Outline each uninfected red blood cell.
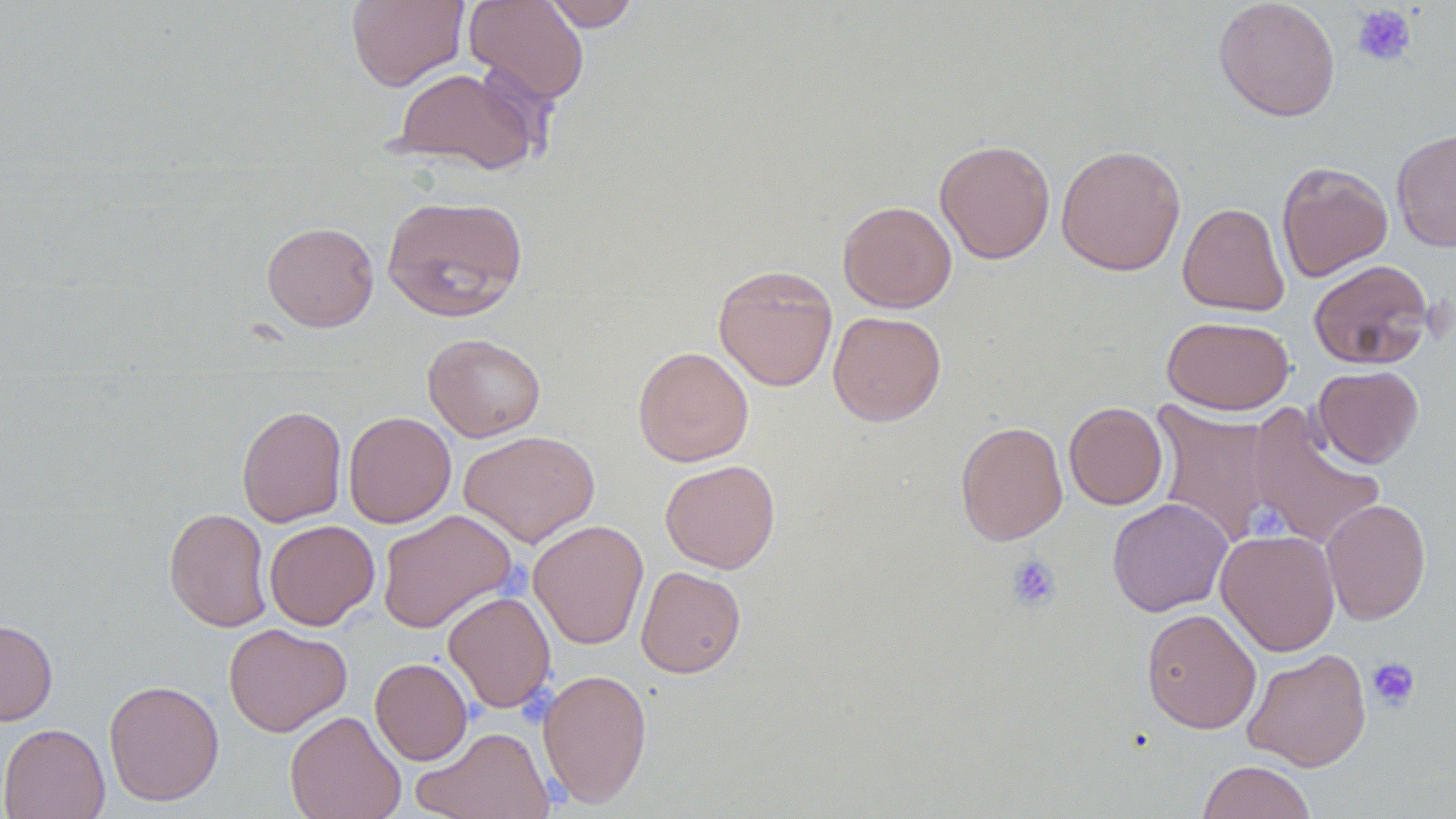
Approximate bounding boxes as named x1/y1/x2/y2 corners in pixels.
Uninfected red blood cells: (x1=346, y1=0, x2=469, y2=91), (x1=464, y1=0, x2=590, y2=105), (x1=540, y1=0, x2=641, y2=31), (x1=1213, y1=0, x2=1341, y2=122), (x1=390, y1=66, x2=542, y2=176), (x1=1391, y1=127, x2=1456, y2=252), (x1=934, y1=138, x2=1056, y2=264), (x1=1056, y1=144, x2=1186, y2=276), (x1=1276, y1=161, x2=1393, y2=282), (x1=381, y1=194, x2=529, y2=322), (x1=838, y1=200, x2=957, y2=313), (x1=1178, y1=202, x2=1290, y2=317), (x1=262, y1=221, x2=379, y2=331), (x1=1308, y1=259, x2=1434, y2=370), (x1=713, y1=264, x2=838, y2=392), (x1=827, y1=311, x2=947, y2=426), (x1=1161, y1=315, x2=1294, y2=415), (x1=423, y1=333, x2=546, y2=441), (x1=633, y1=346, x2=754, y2=467), (x1=1313, y1=365, x2=1424, y2=468), (x1=1150, y1=398, x2=1277, y2=548), (x1=1064, y1=402, x2=1168, y2=510), (x1=236, y1=404, x2=347, y2=527), (x1=1246, y1=405, x2=1386, y2=552), (x1=343, y1=411, x2=456, y2=528), (x1=955, y1=420, x2=1068, y2=545), (x1=459, y1=430, x2=600, y2=548), (x1=660, y1=459, x2=781, y2=573), (x1=1107, y1=497, x2=1232, y2=617), (x1=1320, y1=498, x2=1431, y2=625), (x1=164, y1=507, x2=272, y2=632), (x1=377, y1=509, x2=517, y2=633), (x1=528, y1=519, x2=649, y2=650), (x1=264, y1=520, x2=380, y2=630), (x1=1216, y1=529, x2=1341, y2=656), (x1=635, y1=566, x2=746, y2=678), (x1=443, y1=590, x2=557, y2=713), (x1=1141, y1=608, x2=1261, y2=734), (x1=0, y1=619, x2=58, y2=726), (x1=223, y1=623, x2=352, y2=737), (x1=1242, y1=648, x2=1372, y2=771), (x1=370, y1=657, x2=472, y2=765), (x1=537, y1=668, x2=653, y2=809), (x1=103, y1=679, x2=224, y2=806), (x1=285, y1=710, x2=407, y2=819), (x1=0, y1=723, x2=110, y2=819), (x1=412, y1=726, x2=555, y2=818), (x1=1197, y1=760, x2=1317, y2=819).

slide-level diagnosis = no evidence of blood parasites
image size = 1456×819 pixels
preparation = thin blood smear
field of view = one of a larger specimen
modality = light microscopy
stain = May-Grünwald-Giemsa
platelet locations = approximate bounding boxes as named x1/y1/x2/y2 corners in pixels: (x1=1351, y1=4, x2=1417, y2=67), (x1=1245, y1=503, x2=1304, y2=546), (x1=1006, y1=554, x2=1062, y2=612), (x1=1366, y1=657, x2=1420, y2=711)
magnification = 1000x